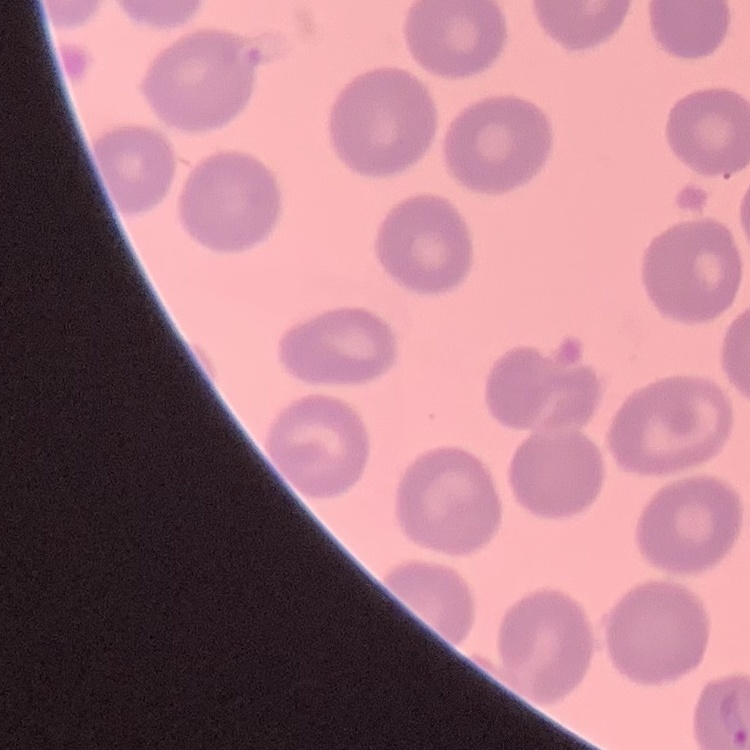
The red blood cells exhibit no rouleaux formation. Field's or Giemsa stain. One tile cut from a larger photomicrograph. Thin peripheral smear.